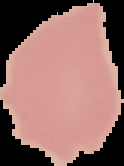 The area outside the segmented cell region is set to black. From a thin blood smear. Image is 124×166 pixels. Malaria status: uninfected.